State which cell type is depicted.
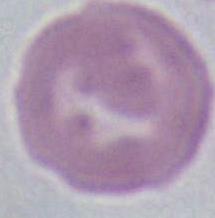

An erythrocyte.

Summary:
  - Magnification: 1000x
  - Modality: micrograph